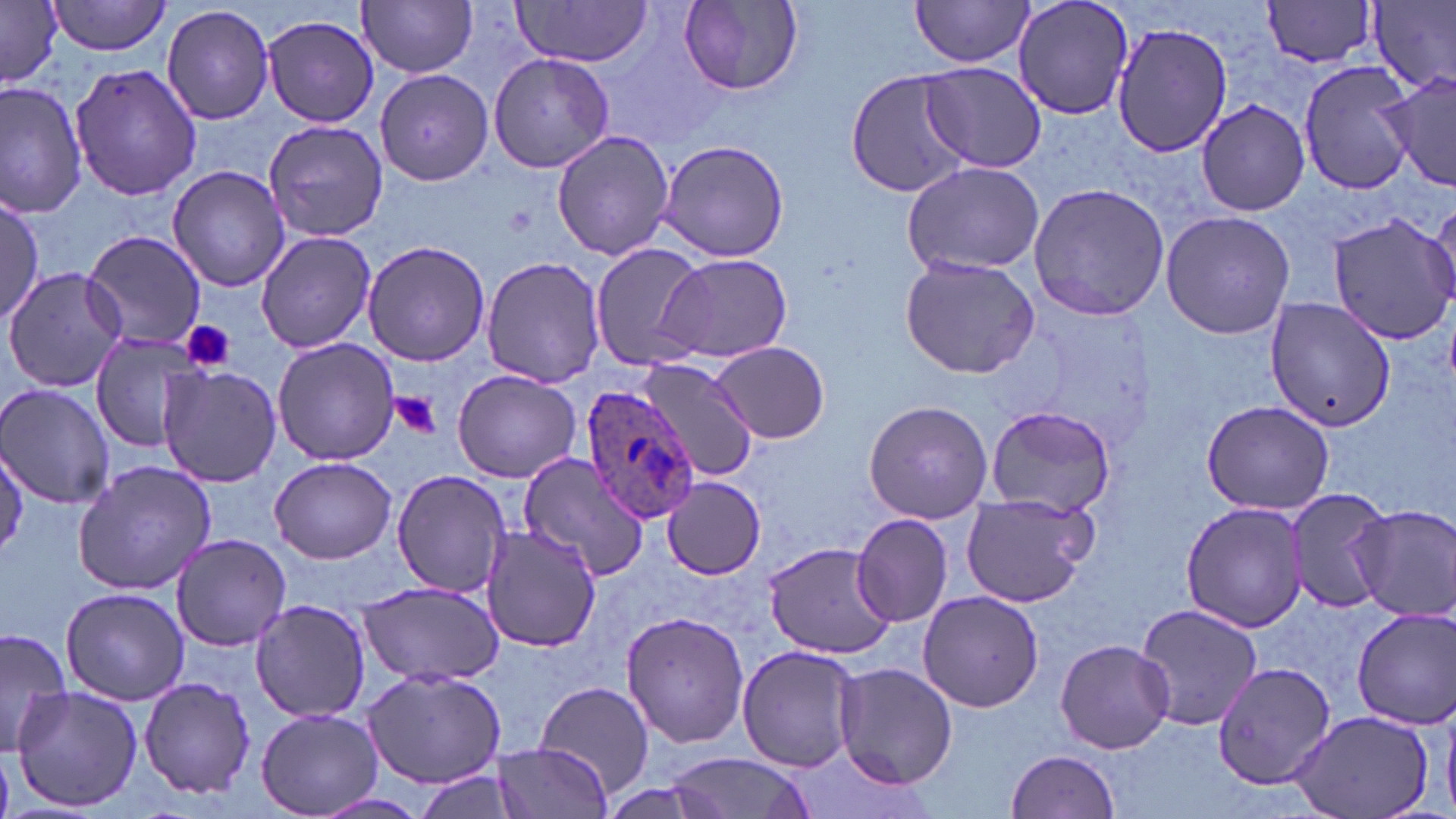
Approximate bounding boxes as [x1, y1, x2, y2] in pixels. Plasmodium ovale-infected red blood cell locations: [579, 385, 701, 526]. Uninfected red blood cell locations: [49, 0, 174, 57], [359, 0, 479, 77], [909, 0, 1036, 68], [1011, 0, 1135, 120], [1260, 0, 1381, 69], [2, 1, 63, 87], [679, 1, 805, 94], [1369, 1, 1455, 95], [507, 3, 654, 67], [161, 4, 275, 127], [262, 13, 380, 127], [1111, 20, 1233, 157], [488, 53, 616, 172], [70, 61, 201, 200], [914, 61, 1046, 173], [1298, 61, 1418, 193], [846, 68, 973, 198], [375, 69, 494, 185], [1383, 72, 1456, 193], [0, 81, 88, 219], [1196, 99, 1311, 216], [261, 119, 388, 242], [551, 130, 675, 262], [658, 139, 789, 262], [900, 160, 1046, 275], [167, 164, 290, 292], [1028, 183, 1172, 322], [0, 193, 43, 326], [1428, 201, 1456, 303], [1159, 209, 1296, 341], [1327, 212, 1456, 345], [81, 229, 206, 350], [255, 231, 376, 353], [363, 239, 490, 366], [588, 242, 709, 371], [658, 253, 794, 365], [899, 254, 1039, 379], [481, 256, 605, 389], [2, 266, 128, 393], [1263, 293, 1394, 433], [88, 330, 209, 452], [271, 338, 399, 465], [710, 341, 830, 443], [635, 358, 762, 480], [158, 366, 283, 487], [451, 370, 583, 484], [0, 384, 114, 508], [863, 399, 993, 524], [1201, 399, 1334, 515], [985, 404, 1117, 519], [518, 452, 648, 580], [270, 456, 397, 563], [72, 460, 217, 595], [392, 469, 514, 598], [662, 477, 765, 580], [1284, 485, 1390, 615], [961, 492, 1100, 607], [1181, 500, 1310, 632], [1350, 503, 1456, 622], [850, 513, 953, 628], [478, 524, 602, 651], [169, 533, 292, 650], [762, 541, 897, 659], [357, 581, 505, 687], [61, 588, 189, 706], [918, 590, 1044, 713], [248, 598, 373, 723], [1134, 602, 1263, 733], [1352, 606, 1455, 728], [621, 610, 750, 749], [0, 627, 73, 759], [1055, 639, 1175, 753], [737, 644, 861, 773], [833, 661, 958, 789], [1212, 661, 1336, 791], [361, 668, 507, 787], [138, 676, 257, 799], [532, 679, 657, 797], [11, 686, 144, 813], [256, 707, 381, 817], [1291, 707, 1436, 818], [490, 742, 614, 817], [1006, 748, 1124, 819], [663, 752, 814, 819], [410, 770, 526, 819], [314, 792, 430, 817]. Platelet locations: [181, 320, 236, 374], [388, 392, 441, 441]. Slide-level diagnosis: Plasmodium ovale. Light microscopy. May-Grünwald-Giemsa stain. Thin blood smear. Image is 1456×819 pixels. 1000x magnification. One field of a larger specimen.